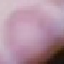
Summary:
  - Result: no malaria parasites detected
  - Capture: smartphone through the microscope eyepiece
  - Stain: Giemsa
  - Image type: automatically extracted cell patch, resized to 64 × 64 pixels
  - Preparation: thin blood smear